Classify this cell by malaria status.
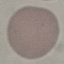

It is uninfected.

image type = cell patch, automatically extracted from a larger field of view and resized to 64 × 64 pixels
capture = smartphone camera at the microscope eyepiece
preparation = thin blood smear
stain = Giemsa